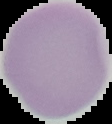

Summary:
  - Image type: segmented cell region on a black background
  - Preparation: thin blood smear
  - Image size: 112×124 pixels
  - Malaria status: uninfected